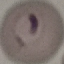
Summary:
  - Malaria status: parasitized
  - Capture: smartphone camera at the microscope eyepiece
  - Stain: Giemsa
  - Preparation: thin smear
  - Image type: cell patch, automatically extracted from a larger field of view and resized to 64 × 64 pixels